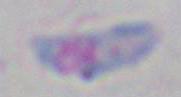
modality = photomicrograph
magnification = 1000x
identification = Toxoplasma gondii